Name the parasite shown.
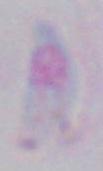
Toxoplasma gondii.

Photomicrograph. 1000x magnification.